Comment on the morphology of the red blood cells.
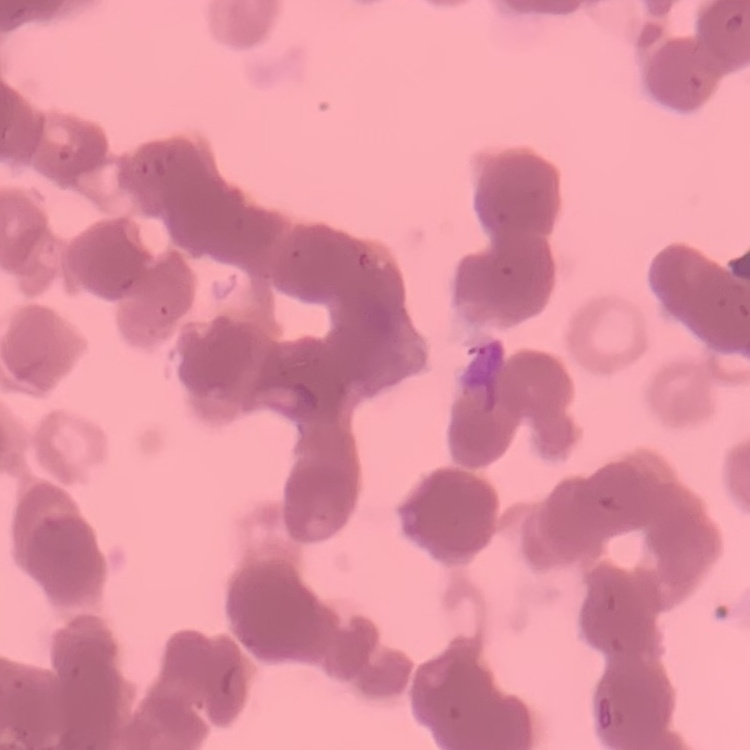
They show rouleaux formation.

image type = one tile cut from a larger photomicrograph
preparation = thin blood smear
stain = Field's or Giemsa